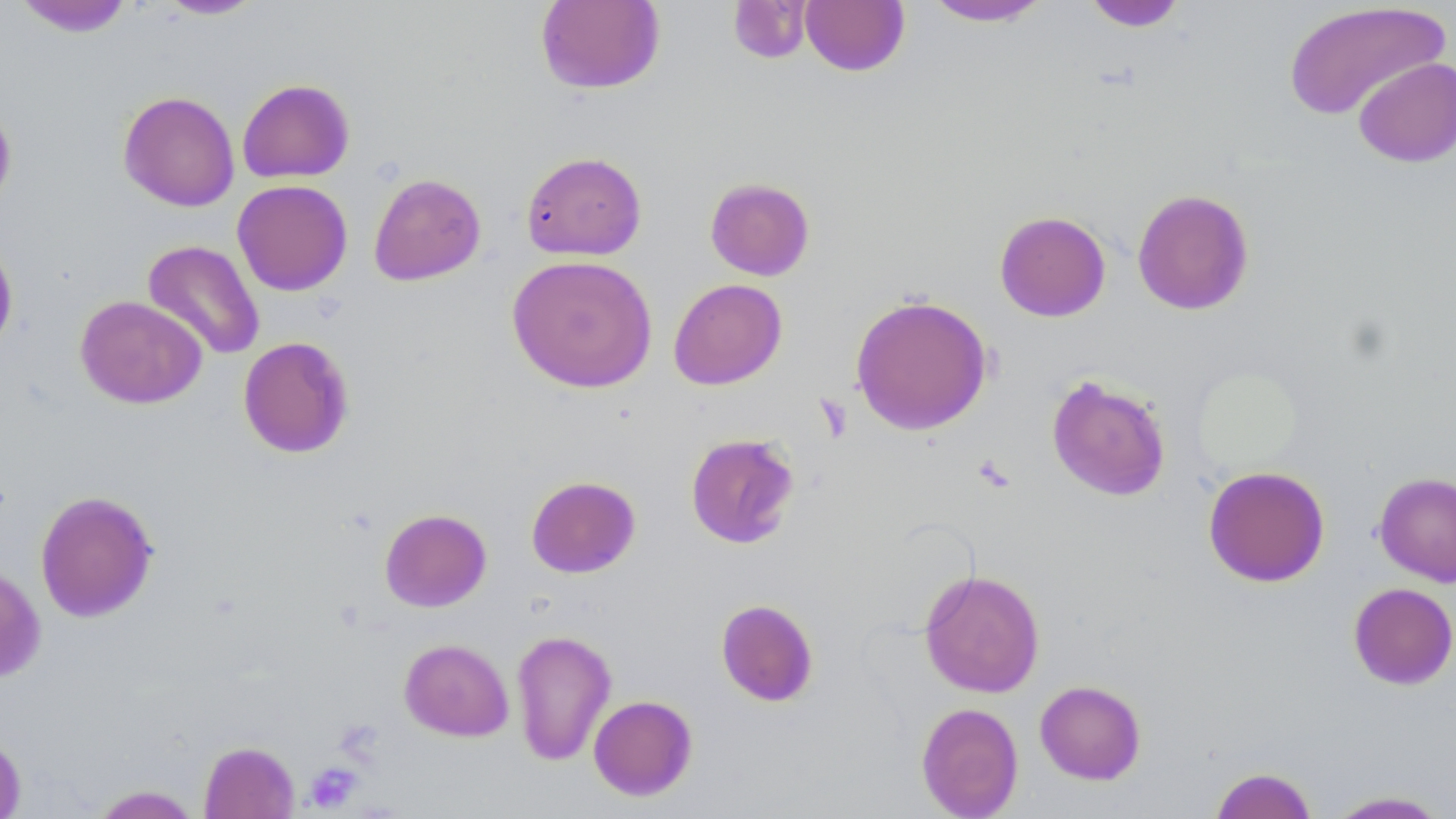
Summary:
  - Coordinate format: approximate bounding boxes as named x1/y1/x2/y2 corners in pixels
  - Platelet locations: (x1=304, y1=762, x2=362, y2=812)
  - Uninfected red blood cell locations: (x1=13, y1=0, x2=134, y2=37), (x1=155, y1=0, x2=266, y2=20), (x1=922, y1=0, x2=1053, y2=27), (x1=535, y1=1, x2=665, y2=94), (x1=728, y1=1, x2=812, y2=63), (x1=799, y1=1, x2=910, y2=76), (x1=1082, y1=1, x2=1188, y2=31), (x1=1281, y1=2, x2=1451, y2=121), (x1=1353, y1=56, x2=1456, y2=167), (x1=237, y1=78, x2=355, y2=183), (x1=118, y1=90, x2=240, y2=212), (x1=0, y1=100, x2=17, y2=212), (x1=521, y1=151, x2=647, y2=260), (x1=368, y1=172, x2=486, y2=286), (x1=705, y1=177, x2=815, y2=280), (x1=232, y1=179, x2=353, y2=296), (x1=1132, y1=188, x2=1254, y2=315), (x1=994, y1=211, x2=1111, y2=322), (x1=0, y1=234, x2=19, y2=355), (x1=142, y1=240, x2=265, y2=361), (x1=507, y1=254, x2=657, y2=393), (x1=668, y1=278, x2=787, y2=389), (x1=850, y1=294, x2=993, y2=436), (x1=75, y1=295, x2=207, y2=409), (x1=238, y1=336, x2=354, y2=458), (x1=1046, y1=374, x2=1171, y2=502), (x1=685, y1=432, x2=800, y2=549), (x1=1203, y1=465, x2=1330, y2=588), (x1=1373, y1=471, x2=1456, y2=586), (x1=526, y1=475, x2=641, y2=578), (x1=35, y1=490, x2=159, y2=623), (x1=379, y1=508, x2=492, y2=612), (x1=0, y1=564, x2=46, y2=682), (x1=919, y1=569, x2=1046, y2=698), (x1=1348, y1=582, x2=1456, y2=690), (x1=715, y1=599, x2=819, y2=707), (x1=510, y1=629, x2=617, y2=766), (x1=399, y1=638, x2=514, y2=742), (x1=1034, y1=679, x2=1146, y2=784), (x1=588, y1=695, x2=698, y2=800), (x1=916, y1=702, x2=1024, y2=818), (x1=0, y1=731, x2=26, y2=819), (x1=199, y1=741, x2=299, y2=818), (x1=1209, y1=766, x2=1319, y2=819), (x1=89, y1=785, x2=202, y2=818), (x1=1323, y1=790, x2=1452, y2=818)
  - Slide-level diagnosis: no evidence of blood parasites
  - Image size: 1456×819 pixels
  - Field of view: one of a larger specimen
  - Preparation: thin blood smear
  - Modality: optical microscopy
  - Magnification: 1000x
  - Stain: May-Grünwald-Giemsa